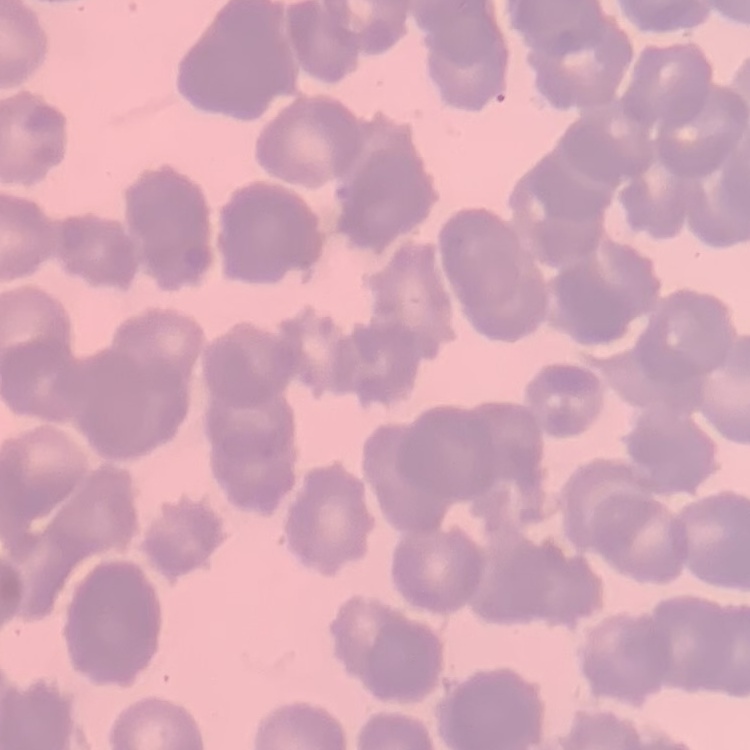

erythrocyte_morphology: rouleaux formation
image_type: one tile cut from a larger photomicrograph
preparation: thin peripheral smear
stain: Field's or Giemsa